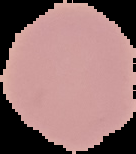
Summary:
  - Image type: segmented cell region with the area outside set to black
  - Result: no Plasmodium parasites seen
  - Preparation: thin blood smear
  - Image size: 136×154 pixels